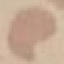

Summary:
  - Result: no malaria parasites detected
  - Capture: smartphone through the microscope eyepiece
  - Image type: automatically extracted cell patch, resized to 64 × 64 pixels
  - Preparation: thin blood film
  - Stain: Giemsa